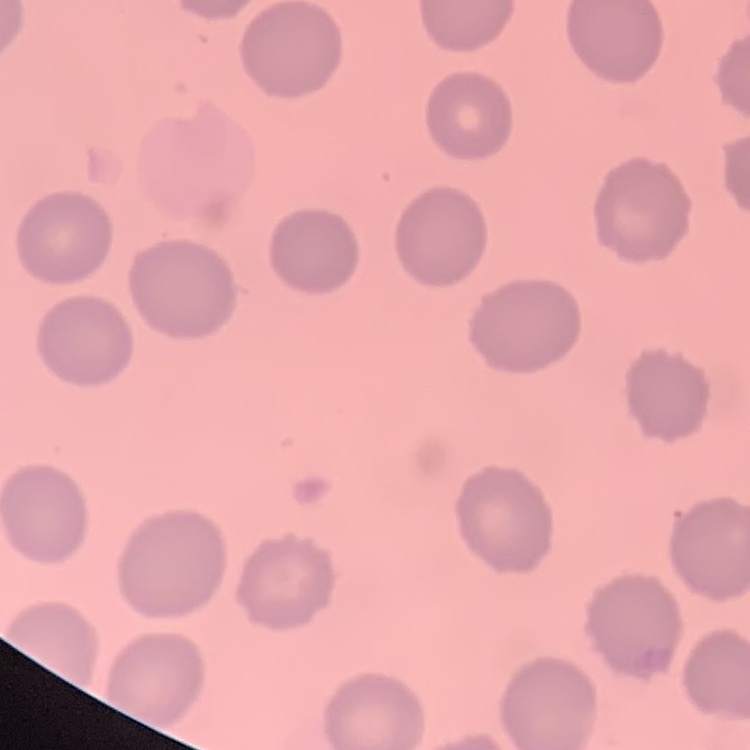
erythrocyte morphology = no rouleaux formation
image type = one tile cut from a larger photomicrograph
preparation = thin peripheral smear
stain = Field's or Giemsa